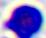
Summary:
  - Magnification: 400x
  - Modality: micrograph
  - Identification: white blood cell